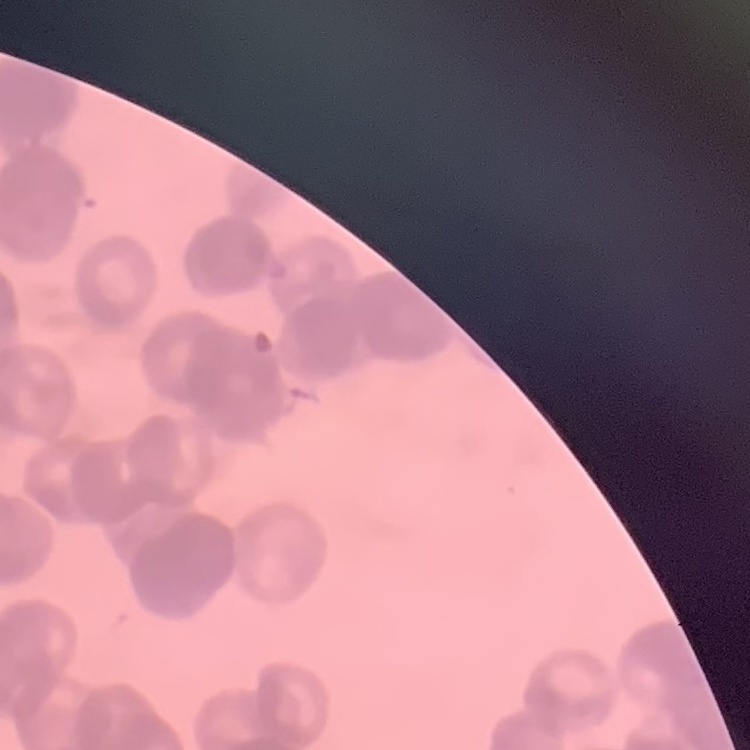
Summary:
  - Red blood cell morphology: rouleaux formation
  - Image type: one tile cut from a larger photomicrograph
  - Preparation: thin blood film
  - Stain: Field's or Giemsa